Name the parasite shown.
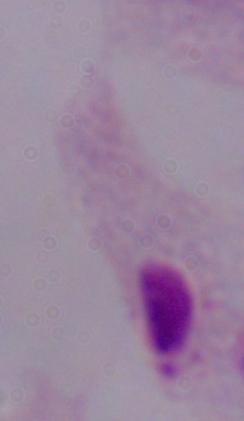
This is a trichomonad.

Photomicrograph. 1000x magnification.